Assess the morphology of the red blood cells.
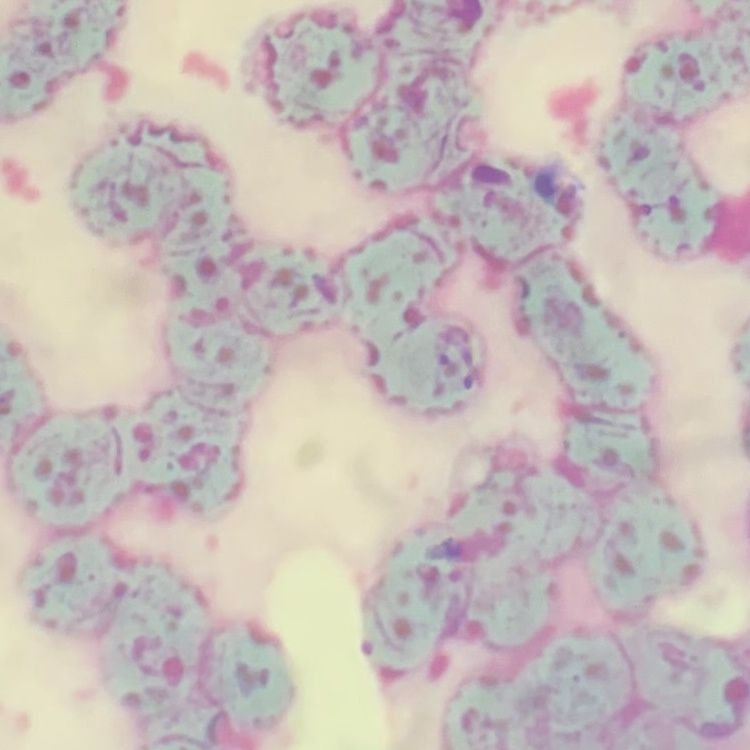

They show rouleaux formation.

Summary:
  - Preparation: thin blood film
  - Image type: one tile cut from a larger photomicrograph
  - Stain: Field's or Giemsa